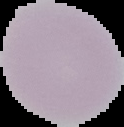
image type = cell region segmented out of the field of view; surrounding area masked to black
preparation = thin blood smear
image size = 124×127 pixels
result = negative for Plasmodium parasites